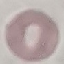

Result: no malaria parasites detected. Cell patch, automatically extracted from a larger field of view and resized to 64 × 64 pixels. Thin blood film. Photographed with a smartphone camera at the microscope eyepiece. Giemsa-stained preparation.